State which parasite is depicted.
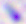

This is Toxoplasma gondii.

Micrograph. Captured at 400x magnification.